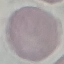

Summary:
  - Malaria status: uninfected
  - Preparation: thin blood smear
  - Capture: smartphone through the microscope eyepiece
  - Image type: cell patch, automatically extracted from a larger field of view and resized to 64 × 64 pixels
  - Stain: Giemsa